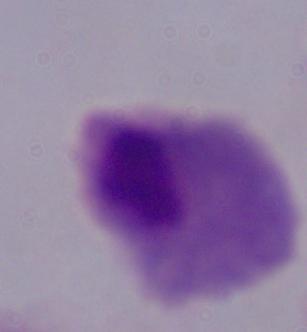

{
  "modality": "photomicrograph",
  "identification": "trichomonad",
  "magnification": "1000x"
}